Classify this cell by malaria status.
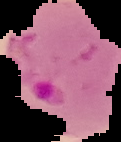
It is parasitized.

image size = 121×142 pixels
image type = segmented cell region on a black background
preparation = thin blood smear